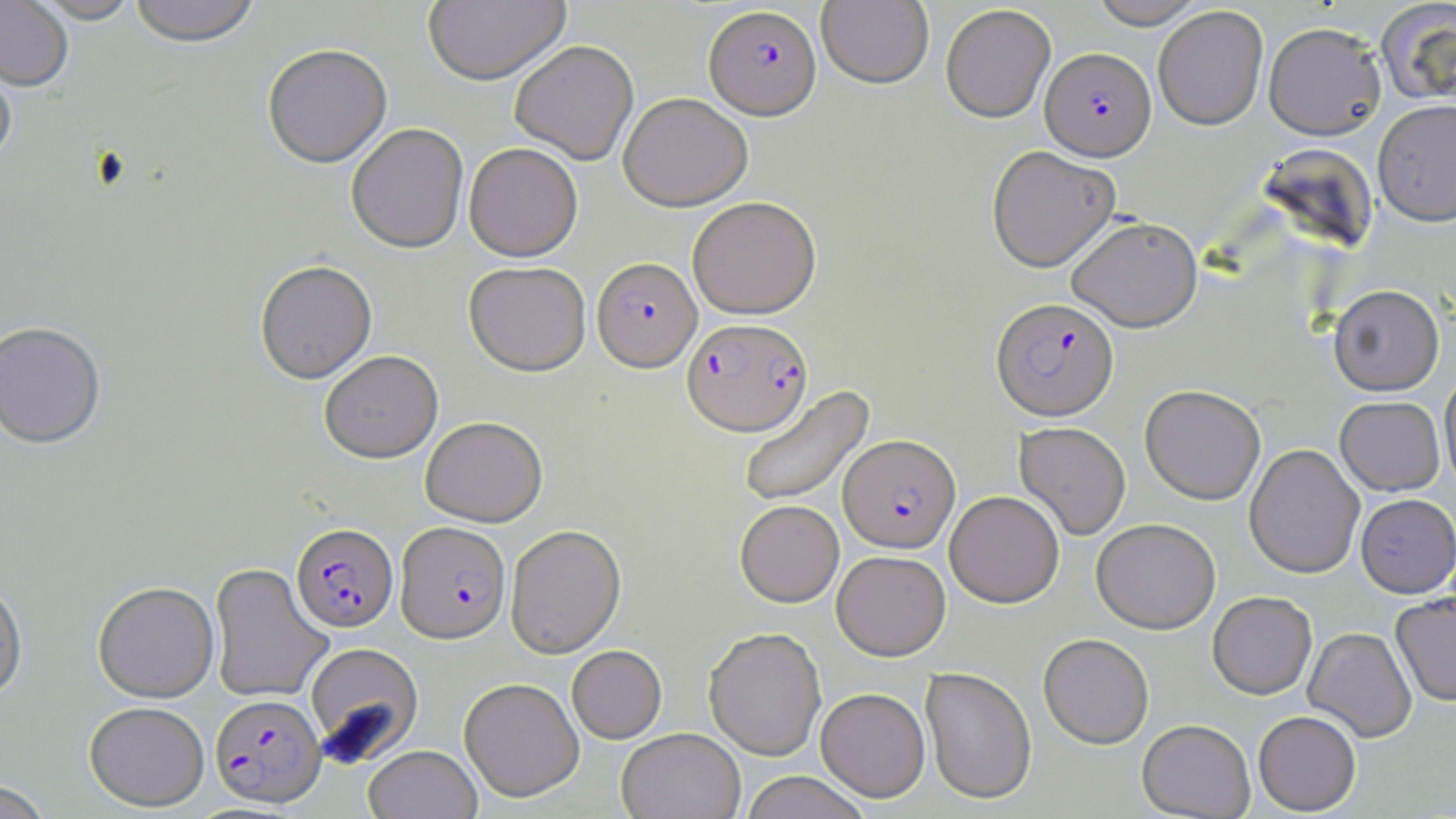
{
  "slide_level_diagnosis": "Plasmodium falciparum",
  "stain": "May-Grünwald-Giemsa",
  "plasmodium_falciparum_infected_red_blood_cell_locations": "approximate bounding boxes as (x1, y1, x2, y2) in pixels: (703, 7, 821, 122), (1041, 47, 1156, 160), (592, 259, 702, 374), (991, 297, 1118, 421), (682, 319, 813, 438), (838, 435, 960, 553), (394, 522, 511, 645), (291, 523, 399, 634), (210, 694, 326, 810)",
  "field_of_view": "single",
  "image_size": "1456×819 pixels",
  "magnification": "1000x",
  "preparation": "thin blood smear",
  "modality": "light microscopy",
  "uninfected_red_blood_cell_locations": "approximate bounding boxes as (x1, y1, x2, y2) in pixels: (0, 0, 73, 93), (30, 0, 142, 26), (128, 0, 261, 51), (424, 0, 571, 88), (817, 0, 934, 90), (1089, 0, 1207, 29), (1377, 2, 1456, 107), (940, 5, 1056, 123), (1153, 6, 1269, 130), (1263, 22, 1386, 141), (510, 42, 639, 166), (262, 46, 392, 170), (0, 57, 17, 172), (618, 95, 753, 213), (1372, 99, 1456, 226), (346, 125, 469, 256), (464, 145, 582, 263), (987, 146, 1120, 273), (687, 197, 822, 320), (1067, 216, 1202, 332), (255, 262, 378, 386), (464, 263, 591, 378), (1328, 285, 1444, 396), (0, 323, 107, 453), (319, 352, 443, 465), (1439, 372, 1456, 494), (738, 384, 875, 510), (1140, 384, 1266, 504), (1335, 396, 1444, 495), (420, 417, 548, 527), (1014, 422, 1131, 540), (1244, 444, 1364, 578), (945, 491, 1065, 608), (1356, 493, 1456, 597), (735, 500, 844, 607), (1092, 518, 1220, 634), (506, 525, 626, 659), (832, 550, 950, 661), (209, 563, 333, 704), (0, 579, 28, 703), (92, 583, 220, 704), (1207, 591, 1317, 700), (1390, 591, 1456, 707), (703, 627, 826, 761), (1303, 627, 1417, 743), (1038, 634, 1154, 749), (304, 643, 423, 765), (567, 645, 667, 744), (919, 667, 1037, 805), (459, 677, 584, 803), (815, 687, 930, 802), (85, 703, 209, 812), (1253, 711, 1361, 816), (1137, 719, 1255, 819), (617, 729, 745, 819), (363, 745, 482, 819), (739, 771, 871, 819), (0, 781, 53, 819)"
}